Point out each Plasmodium parasite.
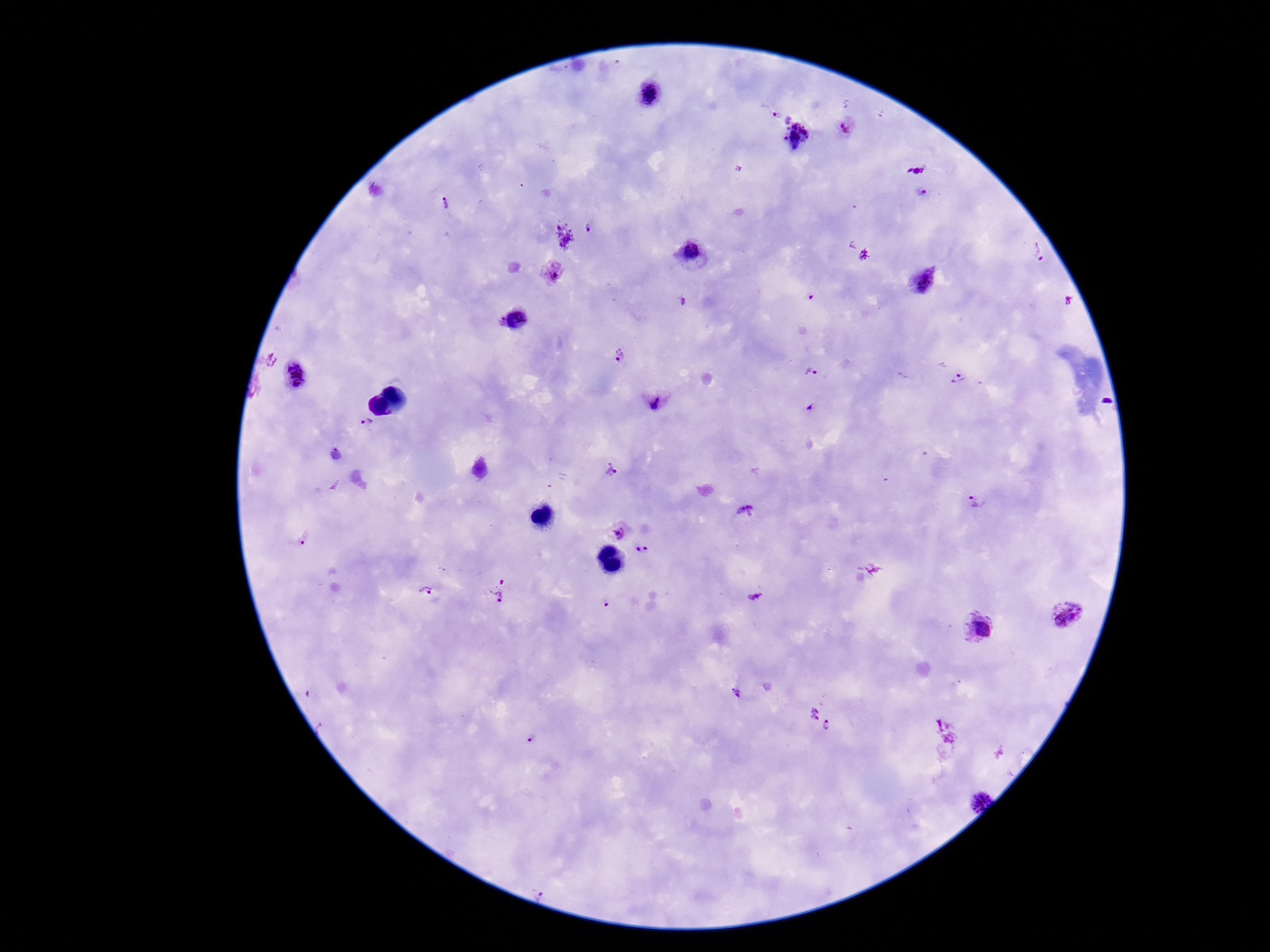

Approximate centers as [x, y] in pixels.
Plasmodium parasites: [649, 95], [780, 115], [848, 128], [797, 129], [922, 192], [446, 204], [591, 228], [1039, 252], [691, 253], [553, 274], [924, 282], [619, 355], [811, 373], [295, 376], [958, 379], [657, 402], [810, 409], [368, 425], [611, 468], [976, 503], [745, 512], [619, 532], [304, 539], [643, 550], [502, 581], [426, 591], [496, 598], [1066, 614], [979, 628], [739, 695], [830, 726], [531, 738], [973, 798], [544, 891].

Summary:
  - Capture: smartphone camera through the microscope eyepiece
  - Preparation: thick peripheral-blood smear
  - Patient malaria status: infected
  - Image size: 1270×952 pixels
  - Field of view: single
  - Magnification: 100x
  - Stain: Giemsa